Identify the blood parasite species.
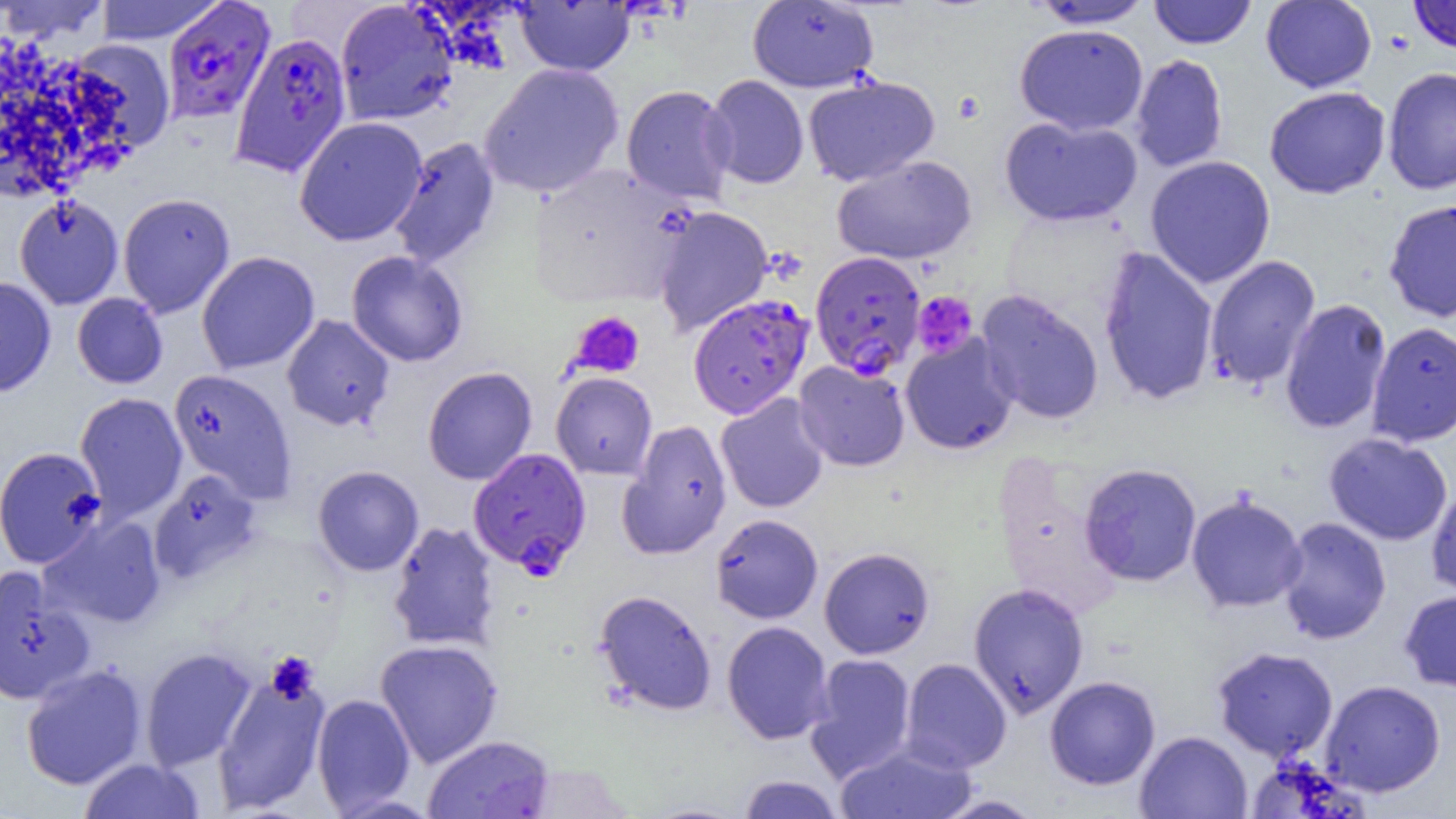
Plasmodium falciparum.

Approximate bounding boxes as [x1, y1, x2, y2] in pixels. Plasmodium falciparum-infected red blood cell locations: [161, 0, 277, 123], [230, 32, 352, 178], [810, 250, 926, 379], [688, 293, 814, 419], [468, 448, 591, 576]. Uninfected red blood cell locations (subset): [1, 0, 109, 43], [93, 0, 224, 44], [1261, 0, 1377, 93], [335, 1, 458, 126], [515, 1, 634, 76], [747, 1, 879, 92], [1027, 1, 1154, 29], [1148, 1, 1257, 49], [1014, 24, 1148, 135], [67, 38, 176, 152], [1130, 54, 1228, 174], [479, 63, 624, 197], [1383, 67, 1456, 195], [704, 75, 809, 189], [802, 75, 940, 186], [621, 84, 737, 205], [1264, 86, 1390, 199], [999, 115, 1143, 227], [294, 116, 428, 246], [387, 137, 500, 269], [831, 155, 977, 265], [1145, 155, 1276, 288], [530, 164, 692, 309], [118, 192, 235, 318], [14, 195, 123, 309], [1384, 198, 1456, 323], [653, 206, 773, 336], [1098, 246, 1219, 406], [196, 251, 320, 374], [346, 251, 468, 367], [1204, 255, 1321, 390], [0, 276, 56, 397], [975, 290, 1104, 425], [72, 293, 168, 388], [1279, 299, 1392, 435], [281, 314, 396, 432], [1366, 321, 1456, 447], [900, 334, 1018, 454], [794, 360, 910, 471], [422, 366, 537, 485], [168, 368, 296, 502], [551, 372, 657, 480], [75, 392, 188, 521], [715, 393, 830, 514], [618, 419, 733, 559], [1324, 433, 1452, 546], [0, 446, 106, 568], [1079, 463, 1202, 587], [312, 465, 424, 576], [149, 469, 264, 584], [1425, 485, 1456, 603], [1186, 493, 1307, 613], [710, 513, 823, 624], [39, 514, 167, 629], [1277, 517, 1392, 644], [387, 521, 501, 652], [819, 547, 934, 659], [0, 565, 95, 705], [968, 583, 1089, 719], [594, 589, 717, 716], [1399, 589, 1456, 692], [721, 621, 834, 744], [375, 639, 503, 768], [1212, 646, 1338, 761], [140, 647, 258, 771], [805, 653, 917, 781], [900, 658, 1012, 773], [20, 663, 147, 790], [212, 666, 331, 815], [1044, 675, 1161, 790], [1320, 680, 1446, 797], [312, 693, 416, 814], [1134, 731, 1252, 819], [423, 734, 554, 819], [835, 741, 978, 818], [79, 758, 205, 818], [737, 774, 845, 818], [933, 795, 1046, 818]. Platelet locations (subset): [912, 291, 978, 359], [568, 311, 645, 379], [265, 651, 319, 703]. One field of a larger specimen. Image is 1456×819 pixels. Captured at 1000x magnification. Light microscopy. Thin blood smear.